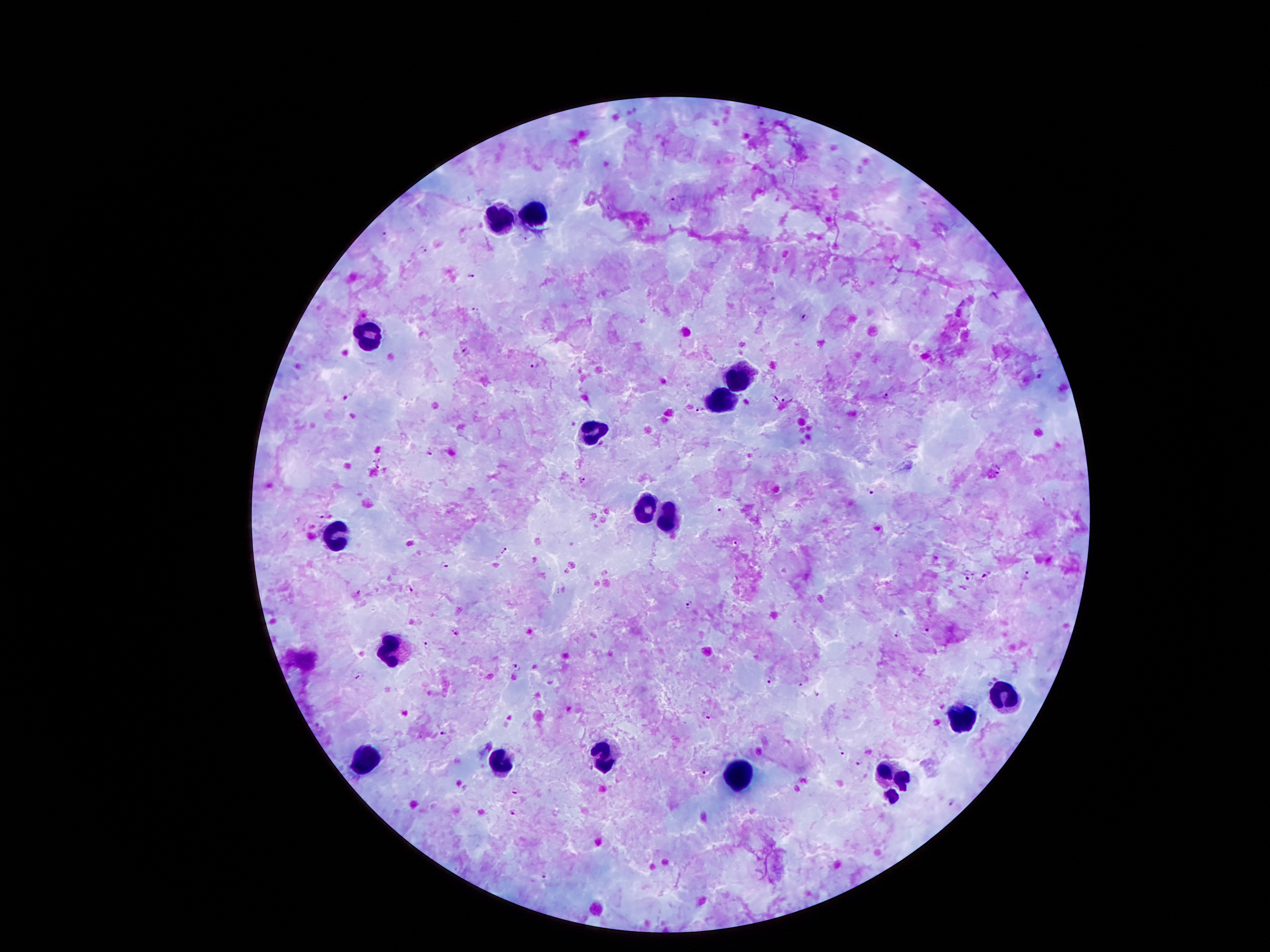
patient_malaria_status: positive for Plasmodium falciparum
leukocyte_locations: 'approximate object centers, in pixels from the top-left corner: (x=533, y=212), (x=502, y=219), (x=372, y=332), (x=739, y=369), (x=728, y=400), (x=595, y=431), (x=646, y=506), (x=666, y=517), (x=341, y=533), (x=389, y=648), (x=1004, y=696), (x=958, y=721), (x=608, y=757), (x=367, y=758), (x=501, y=760), (x=886, y=772), (x=738, y=775), (x=901, y=780), (x=894, y=794)'
field_of_view: one from this slide
preparation: thick peripheral-blood smear
magnification: 100x
malaria_parasite_locations: 'approximate object centers, in pixels from the top-left corner: (x=673, y=198), (x=384, y=234), (x=525, y=238), (x=423, y=249), (x=471, y=277), (x=475, y=308), (x=802, y=319), (x=466, y=350), (x=536, y=364), (x=886, y=397), (x=774, y=399), (x=785, y=399), (x=699, y=407), (x=429, y=454), (x=378, y=462), (x=998, y=471), (x=583, y=481), (x=870, y=491), (x=1044, y=501), (x=722, y=512), (x=325, y=516), (x=737, y=543), (x=505, y=551), (x=443, y=566), (x=1028, y=575), (x=984, y=577), (x=970, y=578), (x=410, y=587), (x=356, y=594), (x=688, y=605), (x=926, y=631), (x=456, y=632), (x=897, y=633), (x=425, y=646), (x=517, y=666), (x=359, y=675), (x=770, y=681), (x=800, y=682), (x=818, y=694), (x=707, y=715), (x=444, y=732), (x=841, y=751), (x=860, y=763), (x=705, y=769), (x=516, y=789), (x=953, y=802), (x=515, y=813), (x=545, y=876)'
image_size: 1270×952 pixels
capture: smartphone through the microscope eyepiece
stain: Giemsa